Comment on the morphology of the erythrocytes.
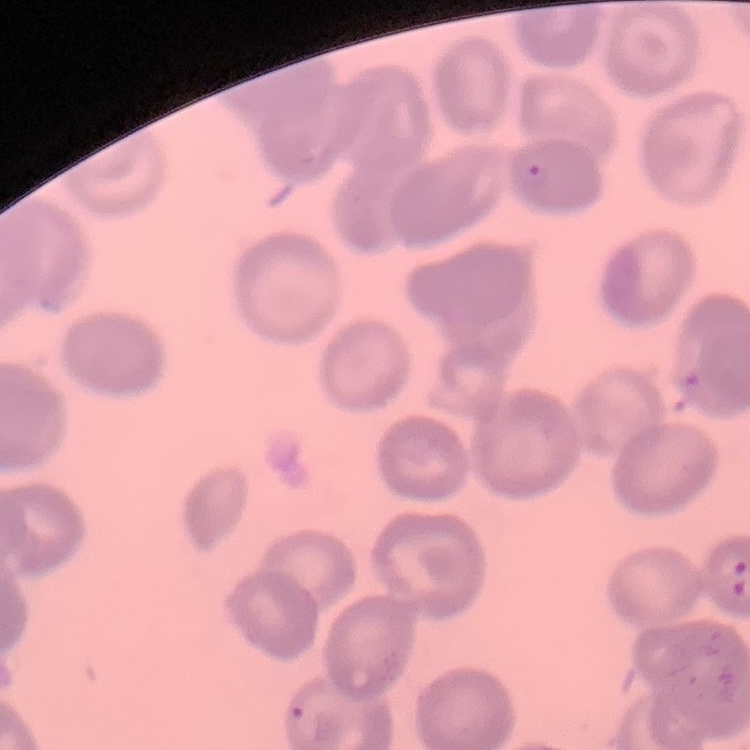

They show no rouleaux formation.

One tile cut from a larger photomicrograph. Thin blood film. Field's or Giemsa stain.